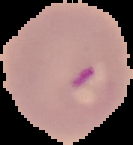
From a thin blood film. Malaria status: parasitized. Segmented cell region on a black background. Image is 133×145 pixels.